Name the parasite shown.
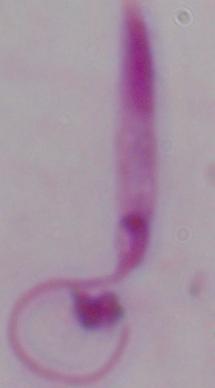
Leishmania.

Captured at 1000x magnification. Photomicrograph.